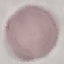

Summary:
  - Result: negative for malaria parasites
  - Capture: smartphone camera at the microscope eyepiece
  - Image type: cell patch, automatically extracted from a larger field of view and resized to 64 × 64 pixels
  - Stain: Giemsa
  - Preparation: thin blood film